State the preparation type.
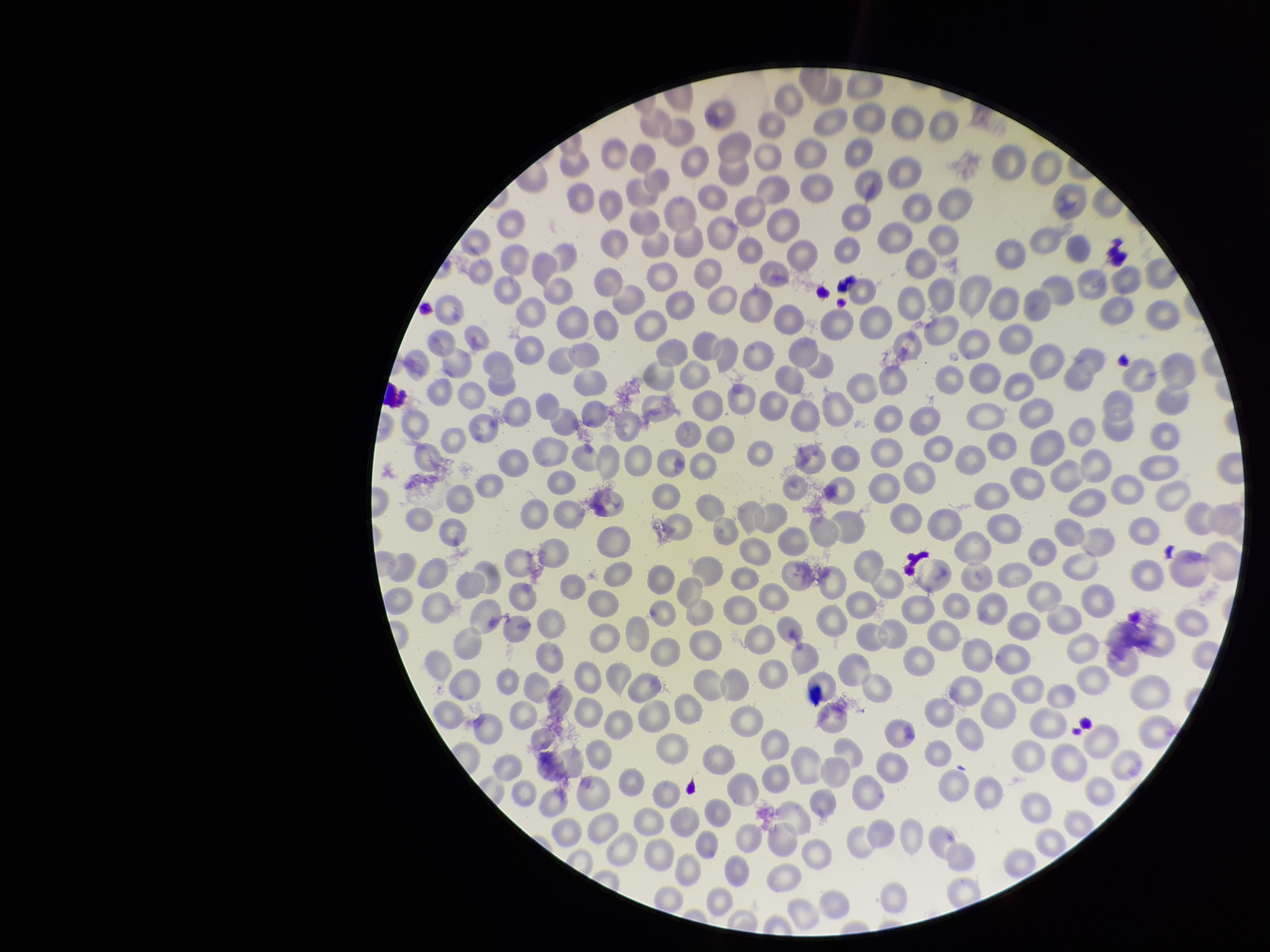

It is a thin blood smear.

{
  "parasitized_red_blood_cell_count": 0,
  "capture": "smartphone photograph through the microscope eyepiece",
  "stain": "Giemsa",
  "parasitized_red_blood_cells": "none seen",
  "field_of_view": "single",
  "patient_malaria_status": "negative",
  "image_size": "1270×952 pixels",
  "red_blood_cell_count": 285
}